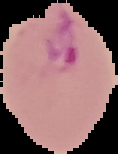
result: Plasmodium parasites identified
preparation: thin blood smear
image_type: cell region segmented out of the field of view; surrounding area masked to black
image_size: 118×154 pixels